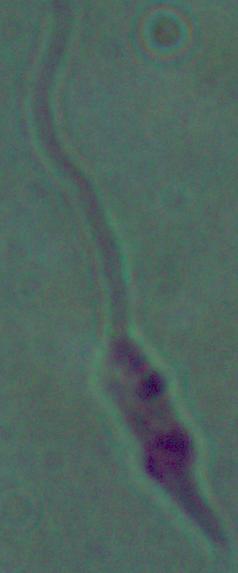 A Leishmania parasite is shown. Photomicrograph. Captured at 1000x magnification.